Report the malaria status of this cell.
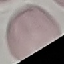

Uninfected.

Summary:
  - Preparation: thin blood film
  - Capture: smartphone through the microscope eyepiece
  - Image type: cell patch, automatically extracted from a larger field of view and resized to 64 × 64 pixels
  - Stain: Giemsa